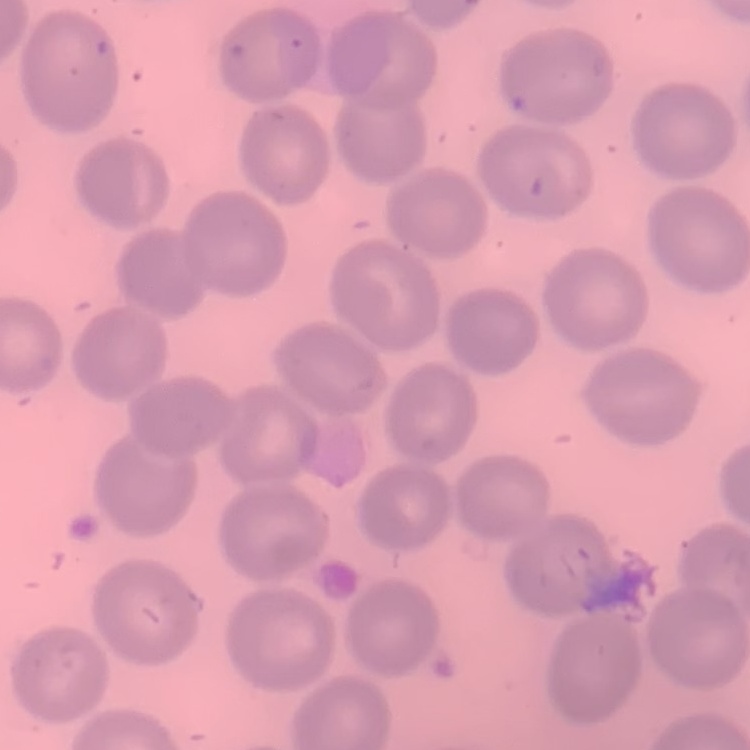
Summary:
  - Erythrocyte morphology: no rouleaux formation
  - Stain: Field's or Giemsa
  - Image type: one tile cut from a larger photomicrograph
  - Preparation: thin peripheral smear